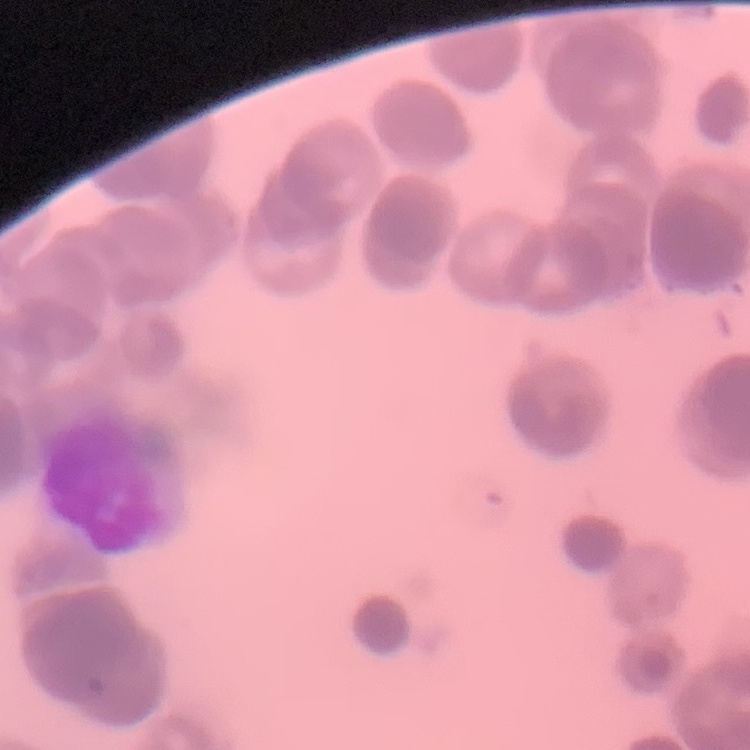

Summary:
  - Red blood cell morphology: rouleaux formation
  - Stain: Field's or Giemsa
  - Image type: one tile cut from a larger photomicrograph
  - Preparation: thin blood film